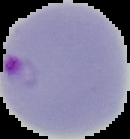
{
  "image_type": "segmented cell region with the area outside set to black",
  "malaria_status": "parasitized",
  "image_size": "130×139 pixels",
  "preparation": "thin blood film"
}